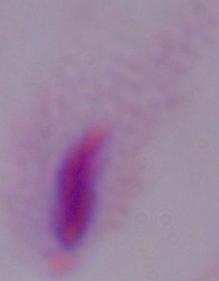
A trichomonad is shown. Micrograph. Captured at 1000x magnification.